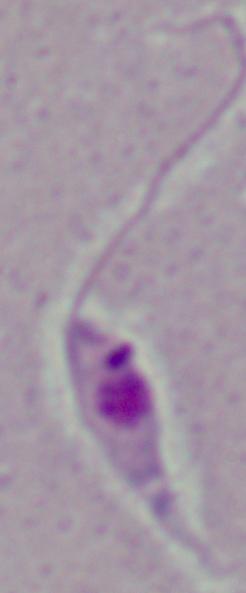

Summary:
  - Identification: Leishmania
  - Magnification: 1000x
  - Modality: micrograph